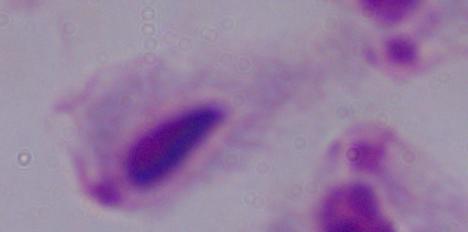

modality = micrograph
magnification = 1000x
identification = trichomonad